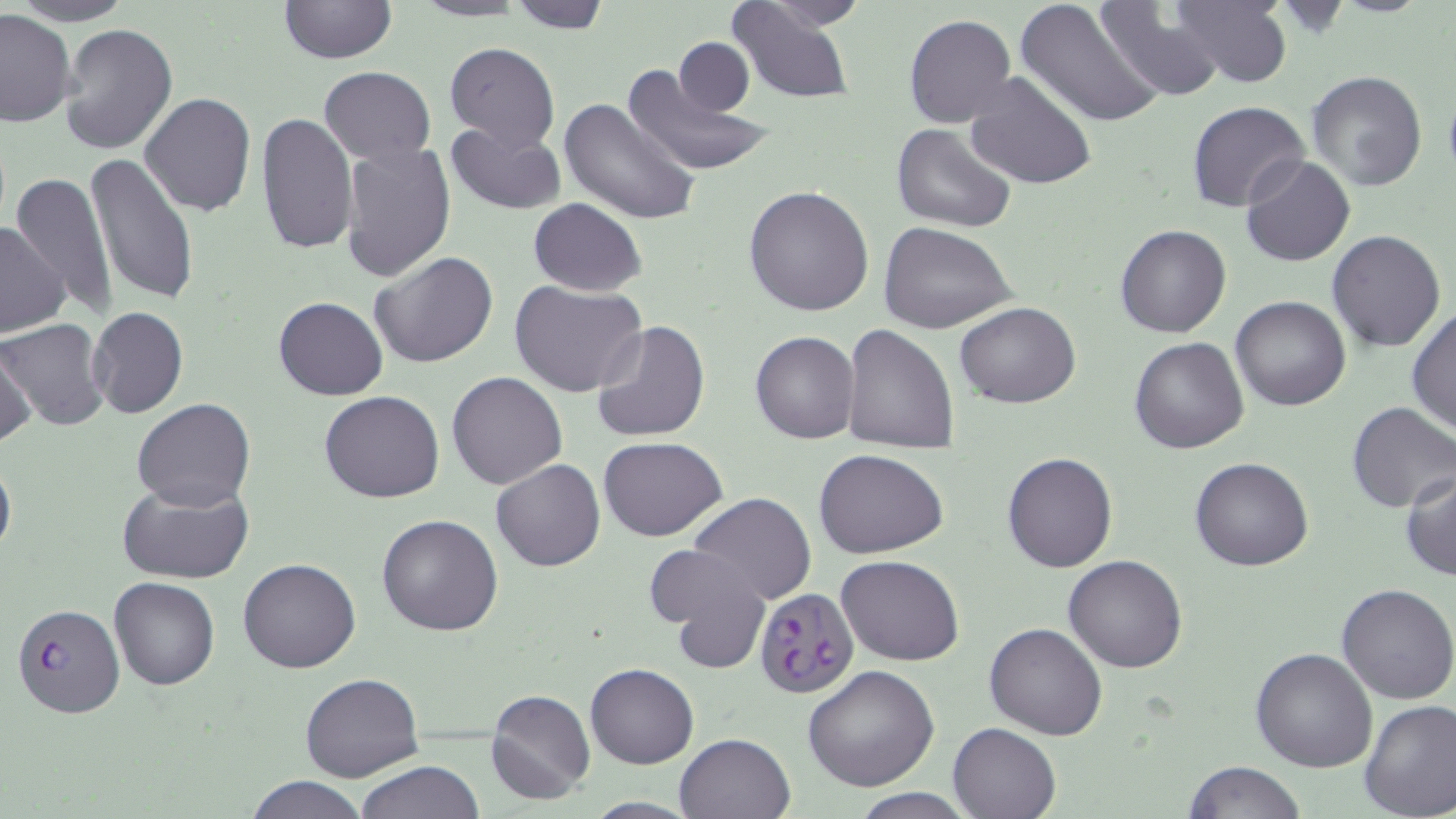

slide-level diagnosis = Plasmodium falciparum
uninfected red blood cell locations = approximate bounding boxes as (x1,y1)-(x2,y2) corner pairs in pixels: (11,0)-(136,25), (277,0)-(397,65), (409,0)-(529,22), (506,0)-(613,32), (751,0)-(871,33), (1014,0)-(1167,128), (1170,0)-(1294,88), (725,1)-(855,105), (1096,4)-(1226,101), (0,9)-(78,126), (904,15)-(1016,128), (59,23)-(178,156), (674,37)-(756,116), (445,41)-(560,150), (622,59)-(771,178), (319,67)-(436,163), (1306,69)-(1428,193), (963,71)-(1096,192), (139,93)-(256,217), (558,96)-(701,226), (1187,102)-(1310,214), (256,110)-(359,256), (446,120)-(566,215), (892,123)-(1018,235), (340,142)-(456,282), (83,153)-(199,309), (1241,155)-(1355,268), (9,174)-(119,321), (743,187)-(875,316), (528,199)-(645,297), (878,222)-(1019,335), (0,224)-(70,337), (1114,224)-(1231,338), (1327,229)-(1446,353), (369,251)-(498,368), (510,280)-(648,398), (1230,295)-(1351,412), (273,297)-(388,401), (954,301)-(1080,409), (87,306)-(188,419), (1406,307)-(1456,436), (1,318)-(110,431), (591,320)-(709,443), (841,324)-(961,452), (750,330)-(860,444), (1130,337)-(1249,454), (0,343)-(36,450), (446,371)-(568,490), (320,390)-(445,503), (133,397)-(255,512), (1346,402)-(1456,513), (598,436)-(728,542), (814,449)-(949,559), (1002,451)-(1118,573), (0,452)-(16,563), (1189,456)-(1314,571), (491,460)-(605,571), (1401,470)-(1456,582), (116,477)-(256,584), (688,493)-(815,606), (376,514)-(502,636), (652,546)-(773,673), (835,555)-(965,667), (1063,555)-(1188,673), (238,558)-(361,673), (108,577)-(219,691), (1336,582)-(1456,703), (984,621)-(1108,739), (1250,647)-(1379,772), (585,662)-(698,769), (803,666)-(938,792), (299,673)-(424,783), (484,687)-(596,805), (1358,699)-(1456,819), (949,722)-(1061,818), (674,732)-(797,819), (356,759)-(484,818), (1185,760)-(1306,818), (246,776)-(368,818), (847,787)-(978,819), (583,796)-(702,817)
image size = 1456×819 pixels
preparation = thin blood smear
magnification = 1000x
Plasmodium falciparum-infected red blood cell locations = approximate bounding boxes as (x1,y1)-(x2,y2) corner pairs in pixels: (754,587)-(860,699), (11,602)-(124,717)
stain = May-Grünwald-Giemsa
field of view = single
modality = optical microscopy